Classify this cell by malaria status.
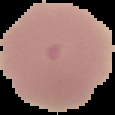
It is uninfected.

image_type: cell region segmented out of the field of view; surrounding area masked to black
preparation: thin blood film
image_size: 115×115 pixels